State which parasite is depicted.
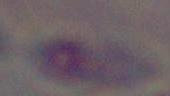

Toxoplasma gondii.

{
  "magnification": "1000x",
  "modality": "photomicrograph"
}